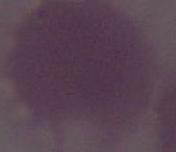 Captured at 1000x magnification. Micrograph. An erythrocyte is seen.